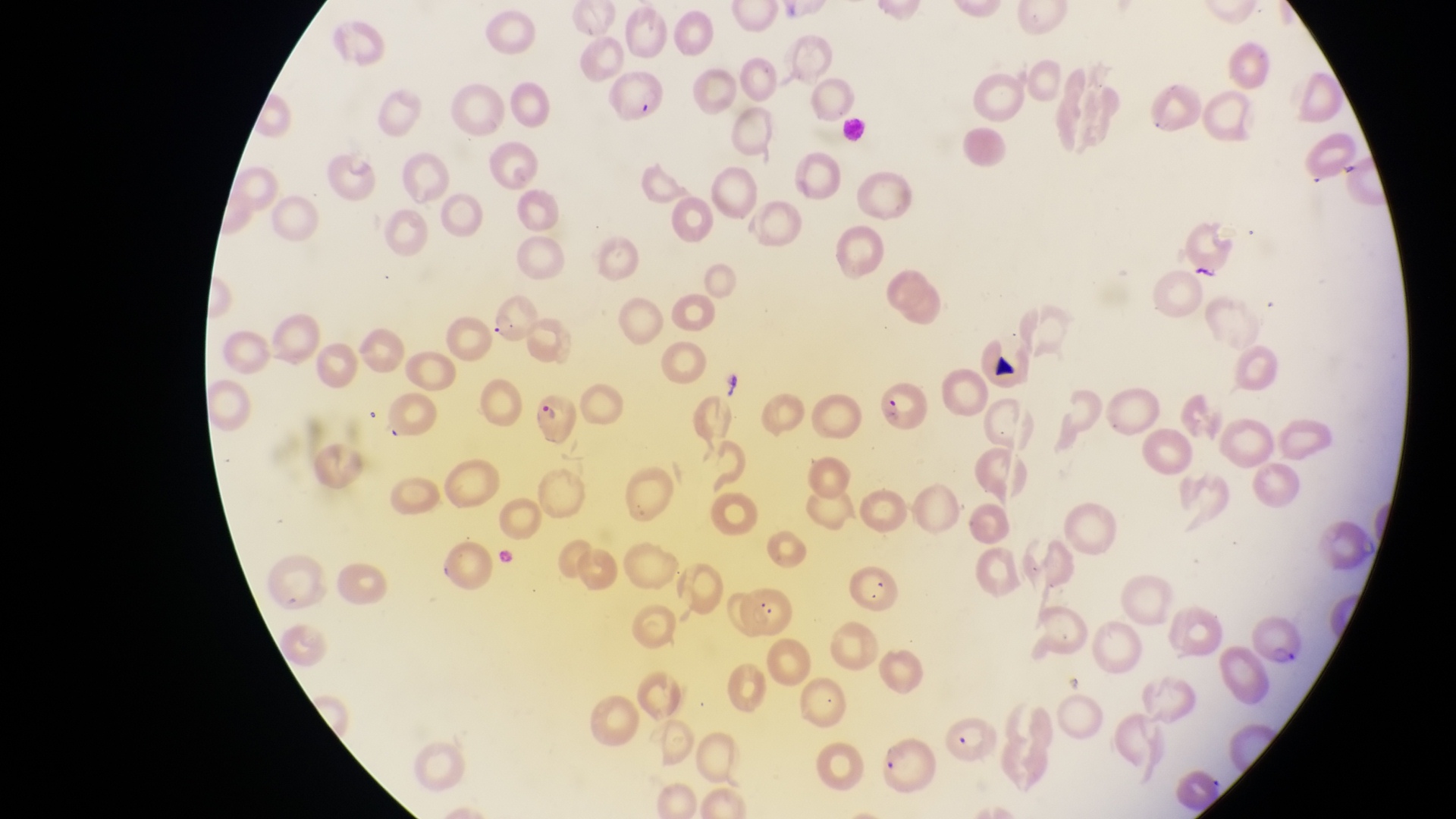

Approximate bounding boxes as [left, top, right, bottom] in pixels.
Summary:
  - Parasitised red blood cell locations: [605, 71, 677, 127], [491, 300, 540, 345], [871, 378, 931, 431], [531, 391, 584, 451], [742, 582, 797, 635], [1252, 616, 1302, 665], [941, 710, 1000, 768], [875, 735, 935, 794]
  - Magnification: 1000x
  - Capture: smartphone photograph through the eyepiece of an Olympus CX-23 microscope
  - Image size: 1456×819 pixels
  - Preparation: thin blood smear
  - Field of view: single
  - Country: Uganda